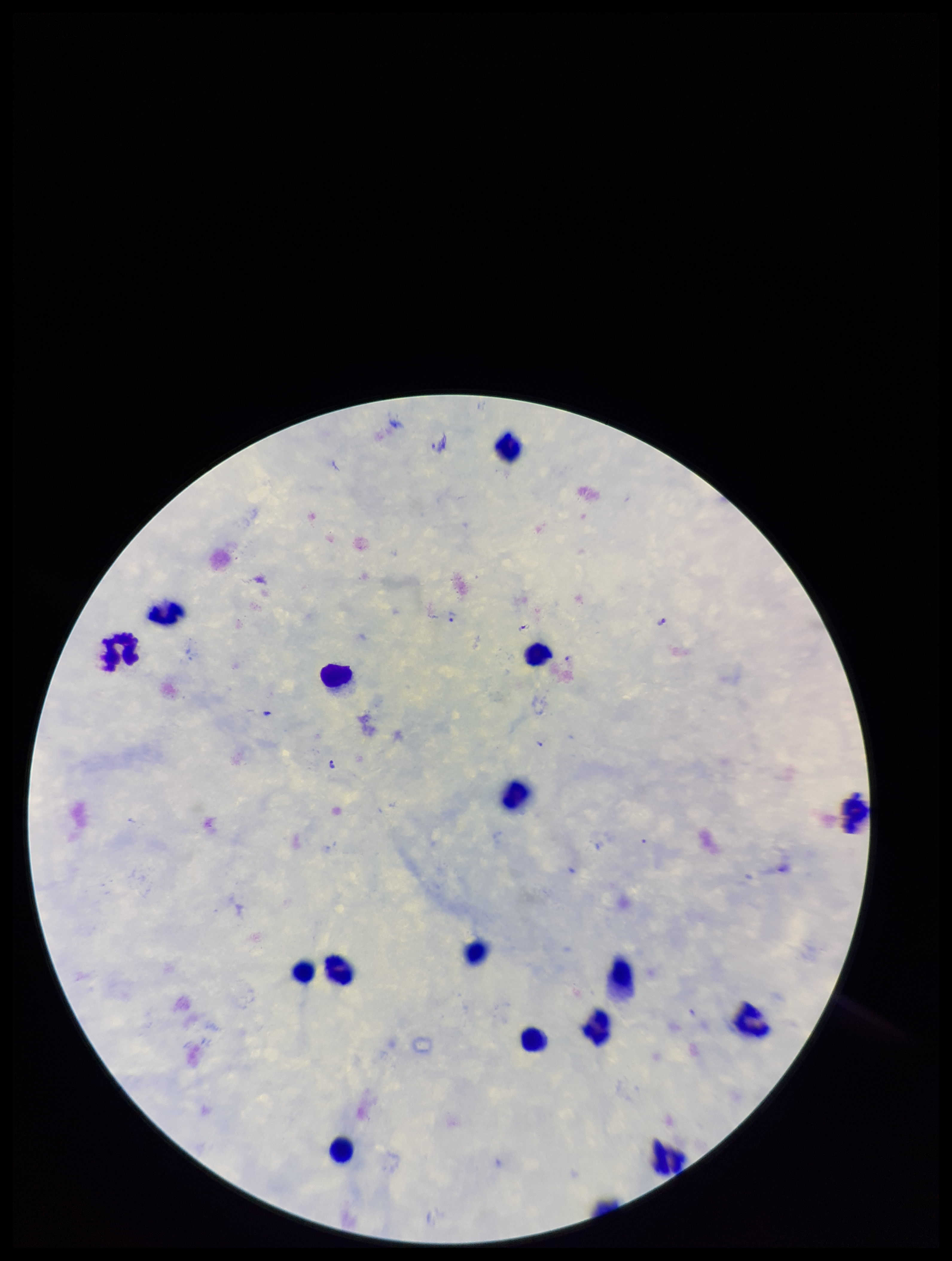

stain = Giemsa
patient malaria status = positive
field of view = single
leukocyte count = 16
species reported for this patient = Plasmodium falciparum
parasite count = 7
Plasmodium parasites = identified
capture = smartphone photograph through the microscope eyepiece
preparation = thick
image size = 952×1261 pixels